Name the parasite shown.
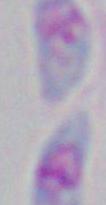

Toxoplasma gondii.

1000x magnification. Micrograph.